Locate and identify every blood parasite.
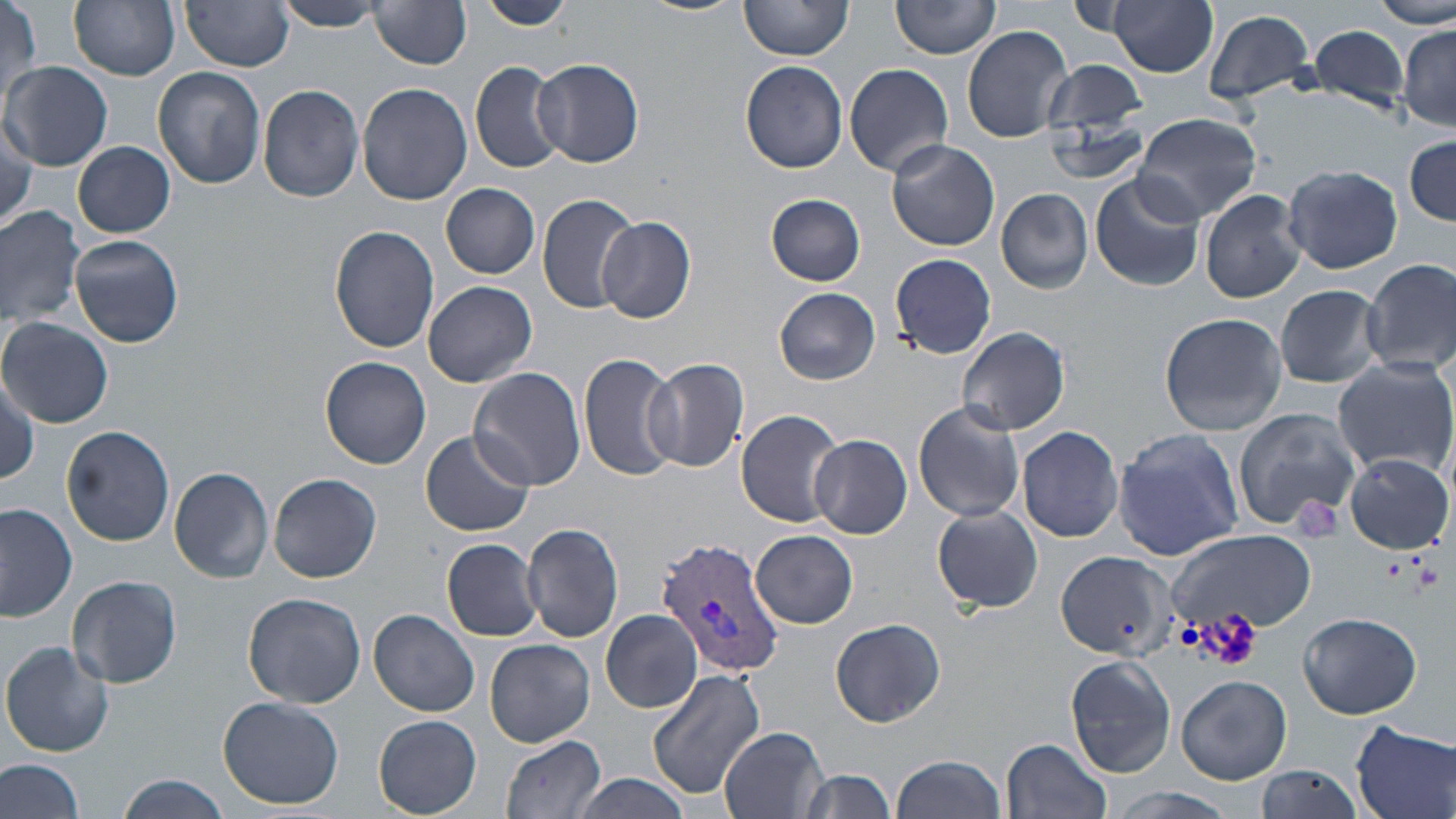

Approximate bounding boxes as [x1, y1, x2, y2] in pixels.
Plasmodium vivax-infected red blood cells: [657, 535, 786, 679].
No Plasmodium falciparum, Plasmodium ovale, Plasmodium malariae, Babesia divergens, or Trypanosoma brucei observed.

slide-level diagnosis = Plasmodium vivax
platelet locations = approximate bounding boxes as [x1, y1, x2, y2] in pixels: [1291, 497, 1345, 544], [1382, 555, 1411, 580], [1411, 562, 1442, 596], [1191, 611, 1266, 673]
field of view = one of a larger specimen
stain = May-Grünwald-Giemsa
image size = 1456×819 pixels
modality = light microscopy
magnification = 1000x
preparation = thin blood smear
uninfected red blood cell locations = approximate bounding boxes as [x1, y1, x2, y2] in pixels: [69, 0, 181, 80], [275, 0, 391, 31], [478, 0, 572, 29], [629, 0, 744, 16], [739, 0, 856, 61], [892, 0, 1002, 59], [1066, 0, 1138, 35], [1107, 0, 1218, 77], [1373, 0, 1454, 27], [184, 2, 294, 72], [370, 2, 474, 70], [2, 3, 42, 102], [1202, 9, 1317, 105], [1308, 22, 1413, 115], [961, 24, 1074, 143], [1399, 24, 1456, 130], [533, 58, 644, 167], [1042, 60, 1150, 144], [470, 61, 567, 176], [740, 61, 848, 173], [2, 62, 113, 171], [845, 62, 954, 176], [153, 67, 266, 189], [356, 83, 472, 207], [258, 84, 364, 202], [1042, 111, 1152, 186], [1130, 112, 1262, 225], [0, 117, 36, 232], [1404, 134, 1455, 224], [887, 138, 1000, 251], [74, 141, 175, 238], [1282, 164, 1402, 275], [1089, 172, 1204, 292], [441, 184, 539, 278], [995, 188, 1093, 293], [1200, 189, 1307, 304], [536, 192, 643, 315], [765, 194, 866, 287], [0, 204, 86, 328], [598, 215, 697, 324], [331, 225, 440, 354], [71, 235, 184, 349], [889, 253, 997, 360], [1360, 258, 1456, 379], [423, 280, 537, 387], [1275, 285, 1384, 387], [773, 288, 880, 385], [1159, 312, 1287, 435], [2, 317, 113, 428], [956, 327, 1070, 435], [580, 353, 680, 483], [321, 356, 431, 468], [644, 356, 750, 472], [1332, 357, 1456, 479], [469, 367, 587, 491], [913, 401, 1026, 523], [1232, 407, 1361, 534], [736, 409, 842, 527], [1017, 426, 1123, 542], [62, 428, 175, 548], [418, 428, 536, 537], [1112, 428, 1244, 561], [810, 433, 912, 538], [1344, 454, 1453, 553], [169, 466, 275, 583], [269, 472, 382, 583], [0, 502, 77, 623], [931, 504, 1045, 613], [521, 521, 625, 643], [1167, 529, 1316, 636], [751, 530, 859, 628], [442, 539, 543, 641], [1055, 548, 1174, 660], [67, 574, 182, 689], [244, 591, 367, 707], [600, 609, 701, 713], [370, 610, 481, 718], [1296, 611, 1423, 719], [829, 617, 946, 727], [485, 638, 593, 748], [1, 642, 114, 758], [1065, 653, 1175, 777], [647, 667, 767, 800], [1176, 674, 1291, 784], [217, 695, 348, 808], [373, 714, 482, 816], [1349, 720, 1456, 819], [719, 728, 829, 819], [500, 734, 606, 819], [1002, 737, 1111, 819], [892, 755, 1005, 819], [0, 757, 88, 819], [1255, 764, 1367, 819], [794, 767, 899, 819], [567, 774, 697, 818], [116, 777, 230, 818], [1106, 787, 1243, 818]